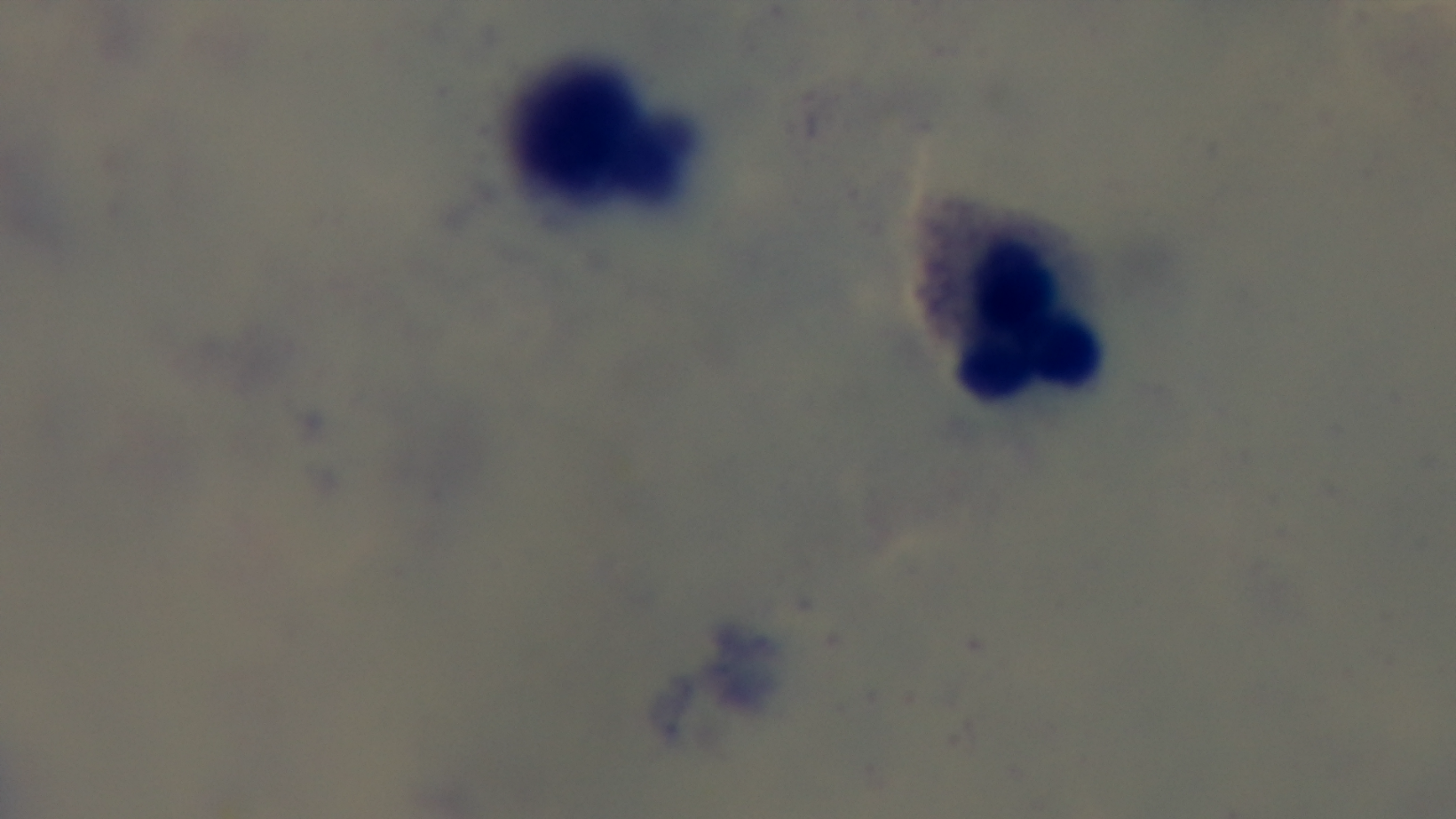

preparation = thick
stain = Giemsa
modality = light microscopy
capture = mounted 4K digital camera
malaria status = negative
field of view = one from the slide
objective = 100x oil immersion